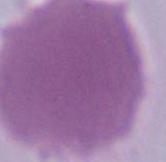

modality = photomicrograph
identification = erythrocyte
magnification = 1000x